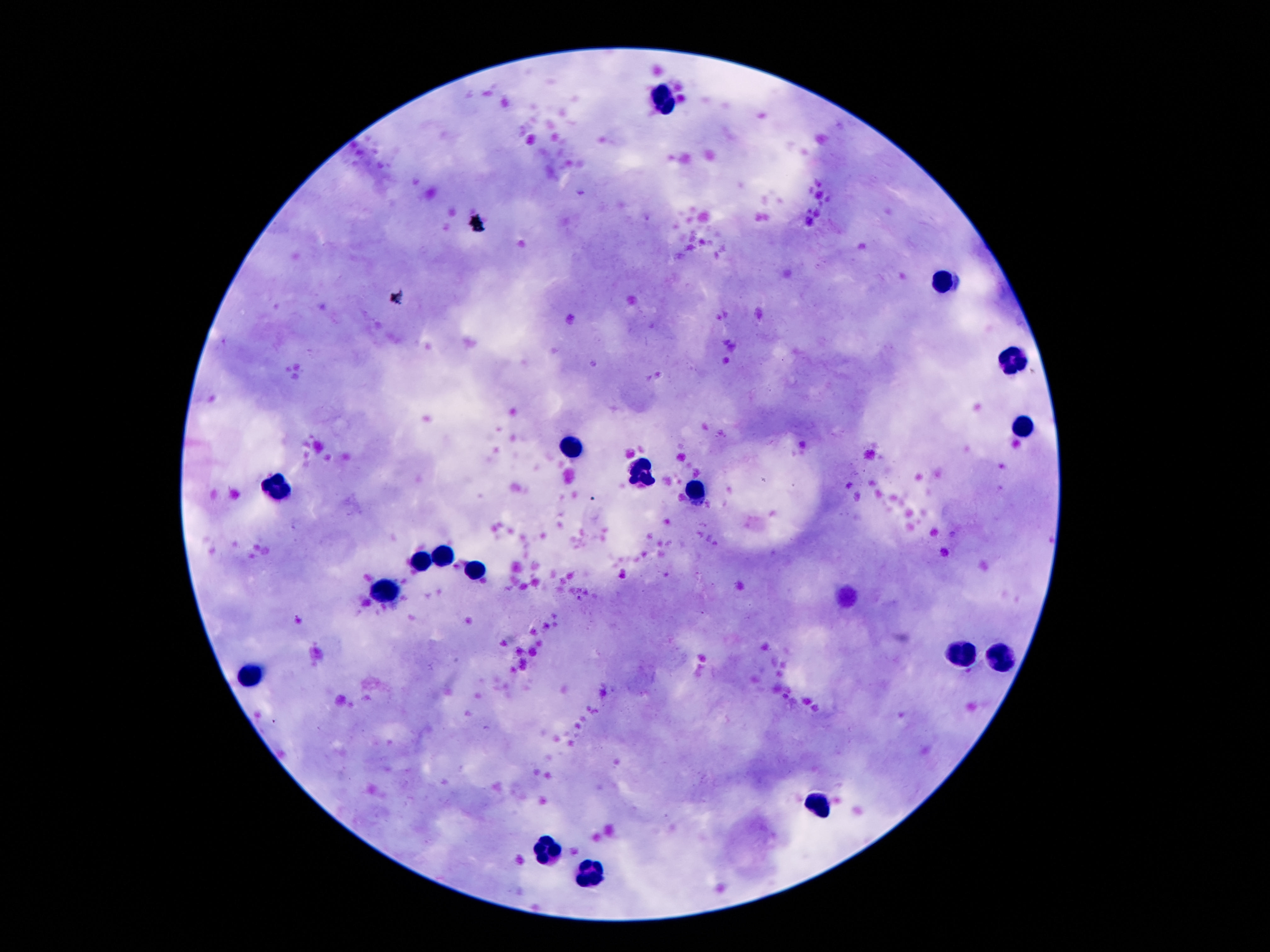

Approximate centers as (x, y) in pixels. Leukocyte locations: (662, 93), (941, 283), (1014, 359), (1023, 424), (571, 445), (643, 472), (278, 490), (696, 490), (444, 556), (423, 563), (473, 572), (385, 592), (959, 654), (1000, 661), (251, 673), (823, 800), (544, 852), (589, 875). Smartphone photograph taken through the microscope eyepiece. Single field of view. Patient malaria status: negative. Image is 1270×952 pixels. Thick blood film. Giemsa stain. 100x magnification.